Outline each blood parasite and name the species.
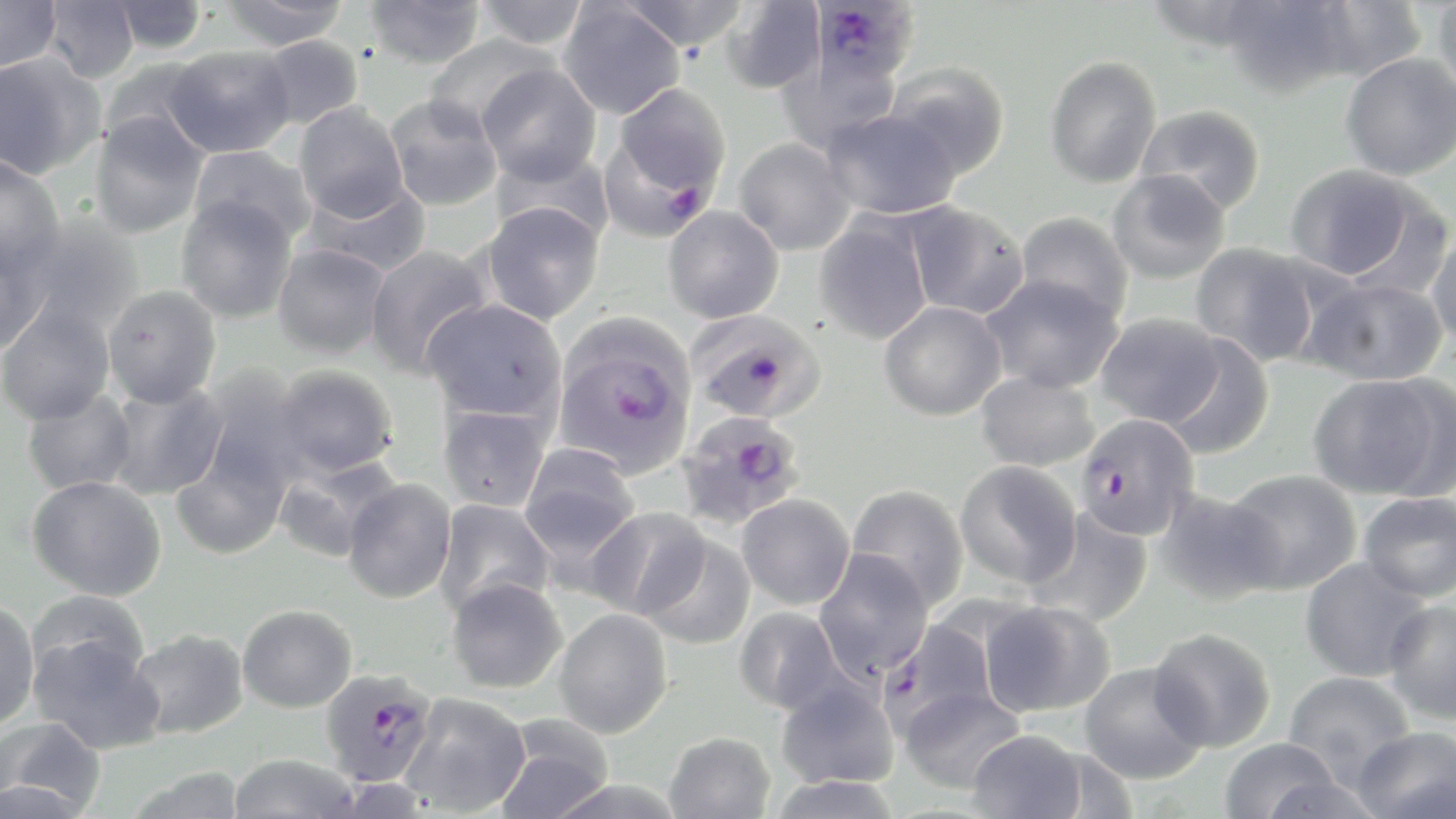
Approximate bounding boxes as named x1/y1/x2/y2 corners in pixels.
Plasmodium falciparum-infected red blood cells: (x1=812, y1=0, x2=919, y2=90), (x1=603, y1=83, x2=731, y2=230), (x1=687, y1=309, x2=826, y2=424), (x1=553, y1=322, x2=697, y2=478), (x1=676, y1=410, x2=807, y2=532), (x1=1075, y1=413, x2=1200, y2=541), (x1=877, y1=618, x2=999, y2=738), (x1=319, y1=668, x2=437, y2=787).
No Plasmodium ovale, Plasmodium malariae, Plasmodium vivax, Babesia divergens, or Trypanosoma brucei observed.

Summary:
  - Uninfected red blood cell locations: (x1=0, y1=0, x2=62, y2=73), (x1=218, y1=0, x2=350, y2=51), (x1=475, y1=0, x2=589, y2=50), (x1=618, y1=0, x2=752, y2=52), (x1=1143, y1=0, x2=1272, y2=52), (x1=1218, y1=0, x2=1357, y2=98), (x1=1306, y1=0, x2=1427, y2=81), (x1=1431, y1=0, x2=1456, y2=103), (x1=42, y1=1, x2=140, y2=83), (x1=109, y1=1, x2=208, y2=54), (x1=363, y1=1, x2=485, y2=69), (x1=719, y1=1, x2=825, y2=95), (x1=558, y1=2, x2=685, y2=120), (x1=423, y1=34, x2=557, y2=136), (x1=254, y1=35, x2=364, y2=130), (x1=164, y1=45, x2=295, y2=158), (x1=1340, y1=53, x2=1456, y2=181), (x1=0, y1=54, x2=104, y2=179), (x1=1045, y1=56, x2=1162, y2=188), (x1=102, y1=58, x2=218, y2=157), (x1=885, y1=62, x2=1011, y2=181), (x1=477, y1=63, x2=602, y2=185), (x1=385, y1=94, x2=503, y2=211), (x1=294, y1=103, x2=409, y2=222), (x1=1135, y1=104, x2=1266, y2=215), (x1=820, y1=107, x2=961, y2=220), (x1=89, y1=112, x2=209, y2=238), (x1=734, y1=138, x2=856, y2=256), (x1=188, y1=145, x2=315, y2=245), (x1=490, y1=148, x2=614, y2=247), (x1=0, y1=157, x2=66, y2=278), (x1=1284, y1=163, x2=1425, y2=283), (x1=1106, y1=170, x2=1231, y2=285), (x1=305, y1=180, x2=432, y2=277), (x1=175, y1=195, x2=298, y2=323), (x1=901, y1=201, x2=1029, y2=320), (x1=481, y1=202, x2=605, y2=325), (x1=662, y1=206, x2=783, y2=324), (x1=1014, y1=212, x2=1134, y2=321), (x1=813, y1=217, x2=933, y2=345), (x1=16, y1=218, x2=145, y2=335), (x1=1426, y1=226, x2=1456, y2=349), (x1=0, y1=238, x2=48, y2=354), (x1=1190, y1=242, x2=1320, y2=366), (x1=363, y1=243, x2=493, y2=377), (x1=272, y1=244, x2=391, y2=358), (x1=980, y1=273, x2=1124, y2=393), (x1=1305, y1=276, x2=1448, y2=386), (x1=102, y1=285, x2=222, y2=407), (x1=422, y1=299, x2=567, y2=424), (x1=0, y1=301, x2=116, y2=425), (x1=879, y1=301, x2=1006, y2=421), (x1=1095, y1=312, x2=1225, y2=428), (x1=1160, y1=333, x2=1275, y2=460), (x1=272, y1=365, x2=398, y2=479), (x1=194, y1=370, x2=313, y2=499), (x1=976, y1=370, x2=1099, y2=472), (x1=1307, y1=374, x2=1451, y2=500), (x1=103, y1=381, x2=227, y2=500), (x1=21, y1=387, x2=138, y2=496), (x1=437, y1=403, x2=552, y2=513), (x1=171, y1=439, x2=291, y2=560), (x1=518, y1=445, x2=641, y2=564), (x1=273, y1=454, x2=401, y2=562), (x1=954, y1=460, x2=1082, y2=589), (x1=1225, y1=469, x2=1362, y2=594), (x1=27, y1=475, x2=167, y2=601), (x1=343, y1=478, x2=457, y2=603), (x1=846, y1=484, x2=970, y2=611), (x1=1154, y1=488, x2=1284, y2=605), (x1=1358, y1=492, x2=1456, y2=603), (x1=737, y1=493, x2=855, y2=609), (x1=435, y1=499, x2=555, y2=617), (x1=585, y1=506, x2=710, y2=620), (x1=1026, y1=509, x2=1153, y2=628), (x1=640, y1=535, x2=756, y2=650), (x1=813, y1=550, x2=934, y2=681), (x1=1299, y1=557, x2=1432, y2=683), (x1=446, y1=576, x2=568, y2=694), (x1=26, y1=591, x2=150, y2=690), (x1=0, y1=598, x2=40, y2=730), (x1=1383, y1=598, x2=1456, y2=724), (x1=980, y1=600, x2=1116, y2=717), (x1=237, y1=604, x2=357, y2=712), (x1=733, y1=606, x2=848, y2=715), (x1=553, y1=608, x2=673, y2=737), (x1=1148, y1=627, x2=1276, y2=752), (x1=126, y1=628, x2=250, y2=740), (x1=30, y1=632, x2=163, y2=754), (x1=1079, y1=662, x2=1208, y2=784), (x1=1282, y1=670, x2=1417, y2=783), (x1=775, y1=677, x2=899, y2=790), (x1=899, y1=686, x2=1026, y2=793), (x1=400, y1=692, x2=533, y2=816), (x1=493, y1=715, x2=615, y2=819), (x1=2, y1=717, x2=106, y2=815), (x1=1351, y1=726, x2=1455, y2=819), (x1=966, y1=728, x2=1087, y2=818), (x1=664, y1=731, x2=775, y2=819), (x1=1218, y1=736, x2=1342, y2=818), (x1=227, y1=753, x2=362, y2=819), (x1=124, y1=766, x2=248, y2=819), (x1=766, y1=775, x2=903, y2=819)
  - Slide-level diagnosis: Plasmodium falciparum
  - Magnification: 1000x
  - Field of view: single
  - Image size: 1456×819 pixels
  - Modality: light microscopy
  - Stain: May-Grünwald-Giemsa
  - Preparation: thin blood film